Name the cell type shown.
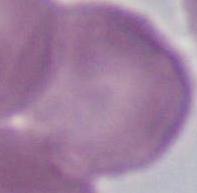

An erythrocyte.

{
  "modality": "micrograph",
  "magnification": "1000x"
}